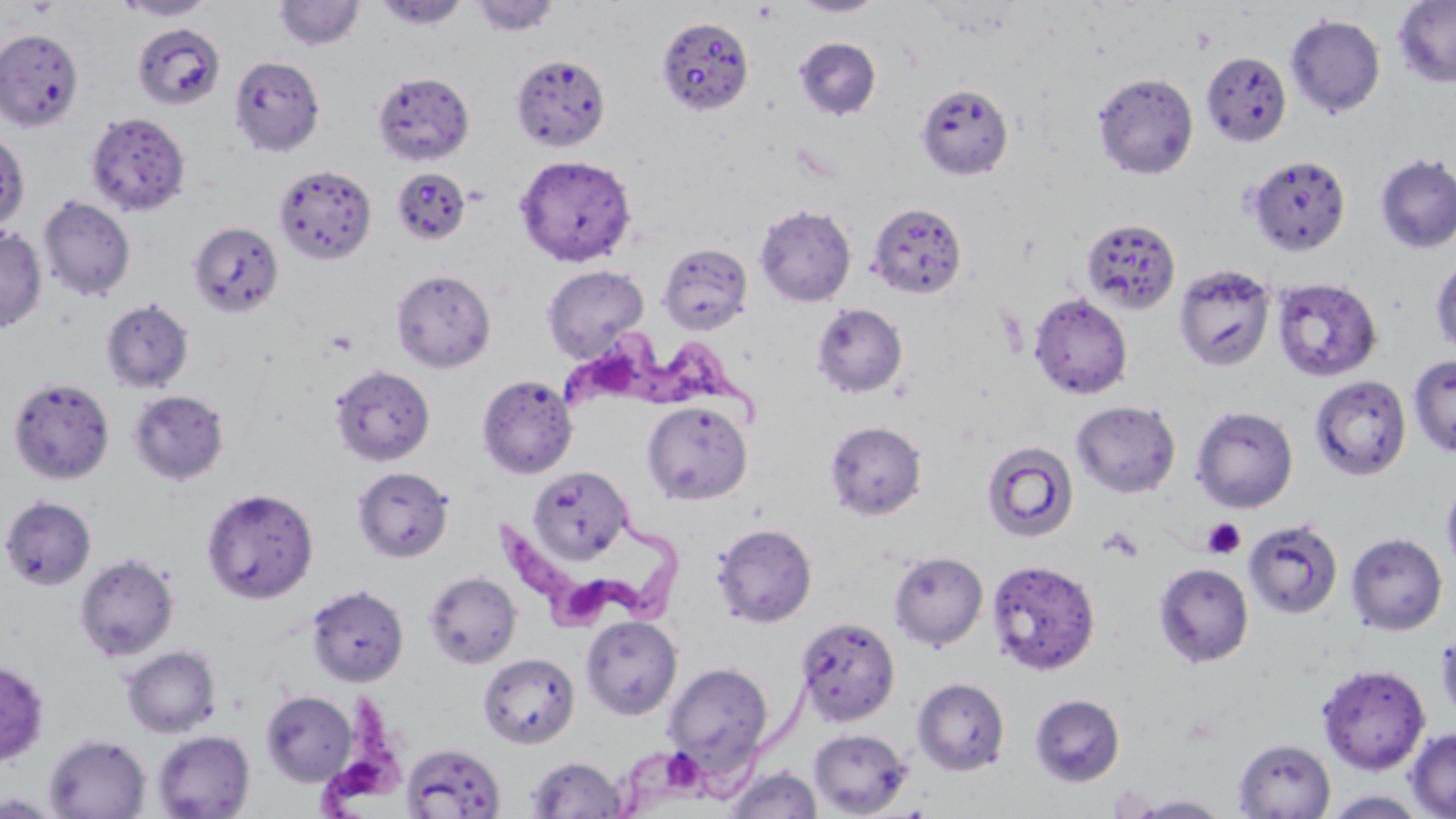
Summary:
  - Coordinate format: approximate bounding boxes as named x1/y1/x2/y2 corners in pixels
  - Platelet locations: (x1=753, y1=3, x2=780, y2=23), (x1=1191, y1=29, x2=1217, y2=54), (x1=326, y1=329, x2=359, y2=356), (x1=1202, y1=517, x2=1247, y2=560), (x1=1100, y1=526, x2=1144, y2=563)
  - Uninfected red blood cell locations: (x1=116, y1=0, x2=216, y2=21), (x1=470, y1=0, x2=561, y2=37), (x1=791, y1=0, x2=887, y2=18), (x1=1392, y1=0, x2=1456, y2=88), (x1=273, y1=1, x2=364, y2=52), (x1=374, y1=1, x2=470, y2=30), (x1=1285, y1=14, x2=1385, y2=117), (x1=655, y1=16, x2=754, y2=118), (x1=133, y1=23, x2=226, y2=110), (x1=0, y1=28, x2=84, y2=131), (x1=794, y1=37, x2=882, y2=120), (x1=1201, y1=51, x2=1292, y2=146), (x1=229, y1=54, x2=326, y2=157), (x1=510, y1=54, x2=611, y2=152), (x1=372, y1=71, x2=474, y2=165), (x1=1092, y1=72, x2=1198, y2=179), (x1=916, y1=83, x2=1014, y2=181), (x1=85, y1=111, x2=191, y2=217), (x1=1, y1=131, x2=29, y2=233), (x1=1374, y1=153, x2=1456, y2=254), (x1=514, y1=154, x2=637, y2=267), (x1=1246, y1=155, x2=1351, y2=255), (x1=273, y1=164, x2=376, y2=264), (x1=391, y1=167, x2=471, y2=245), (x1=38, y1=195, x2=136, y2=302), (x1=866, y1=202, x2=967, y2=298), (x1=754, y1=204, x2=856, y2=307), (x1=1081, y1=218, x2=1181, y2=314), (x1=189, y1=220, x2=284, y2=318), (x1=0, y1=228, x2=47, y2=332), (x1=657, y1=242, x2=752, y2=335), (x1=1431, y1=257, x2=1456, y2=356), (x1=1174, y1=263, x2=1276, y2=372), (x1=541, y1=264, x2=649, y2=362), (x1=391, y1=269, x2=496, y2=372), (x1=1272, y1=278, x2=1382, y2=382), (x1=1028, y1=292, x2=1133, y2=399), (x1=101, y1=299, x2=193, y2=393), (x1=811, y1=303, x2=908, y2=398), (x1=1408, y1=355, x2=1456, y2=457), (x1=330, y1=365, x2=435, y2=466), (x1=477, y1=374, x2=578, y2=479), (x1=1310, y1=375, x2=1411, y2=480), (x1=8, y1=377, x2=114, y2=484), (x1=127, y1=390, x2=230, y2=485), (x1=1072, y1=400, x2=1180, y2=497), (x1=642, y1=401, x2=752, y2=505), (x1=1191, y1=405, x2=1298, y2=513), (x1=825, y1=420, x2=927, y2=520), (x1=981, y1=440, x2=1079, y2=542), (x1=352, y1=466, x2=454, y2=562), (x1=528, y1=467, x2=633, y2=563), (x1=1441, y1=474, x2=1456, y2=578), (x1=201, y1=487, x2=318, y2=603), (x1=1, y1=495, x2=97, y2=590), (x1=1243, y1=518, x2=1343, y2=619), (x1=712, y1=523, x2=817, y2=628), (x1=1346, y1=532, x2=1447, y2=635), (x1=888, y1=551, x2=988, y2=650), (x1=74, y1=553, x2=179, y2=662), (x1=992, y1=561, x2=1102, y2=672), (x1=1154, y1=563, x2=1254, y2=668), (x1=423, y1=571, x2=521, y2=668), (x1=306, y1=585, x2=409, y2=687), (x1=580, y1=615, x2=682, y2=721), (x1=795, y1=616, x2=900, y2=726), (x1=1436, y1=625, x2=1456, y2=723), (x1=120, y1=645, x2=221, y2=738), (x1=478, y1=652, x2=580, y2=748), (x1=0, y1=660, x2=49, y2=766), (x1=662, y1=662, x2=774, y2=778), (x1=1317, y1=663, x2=1430, y2=775), (x1=912, y1=677, x2=1010, y2=776), (x1=261, y1=691, x2=358, y2=785), (x1=1030, y1=694, x2=1125, y2=786), (x1=1405, y1=727, x2=1456, y2=818), (x1=808, y1=728, x2=913, y2=817), (x1=152, y1=730, x2=255, y2=819), (x1=44, y1=734, x2=151, y2=818), (x1=1233, y1=738, x2=1336, y2=818), (x1=401, y1=743, x2=506, y2=819), (x1=526, y1=755, x2=626, y2=818), (x1=723, y1=766, x2=823, y2=819), (x1=1321, y1=790, x2=1430, y2=818), (x1=0, y1=793, x2=62, y2=818), (x1=1123, y1=793, x2=1232, y2=818)
  - Trypanosoma brucei locations: (x1=554, y1=334, x2=770, y2=422), (x1=495, y1=510, x2=697, y2=631), (x1=617, y1=660, x2=846, y2=813), (x1=314, y1=692, x2=405, y2=818)
  - Slide-level diagnosis: Trypanosoma brucei
  - Modality: optical microscopy
  - Stain: May-Grünwald-Giemsa
  - Preparation: thin blood film
  - Magnification: 1000x
  - Image size: 1456×819 pixels
  - Field of view: one of a larger specimen